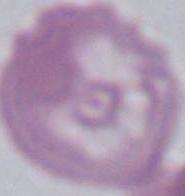
identification: red blood cell
magnification: 1000x
modality: micrograph